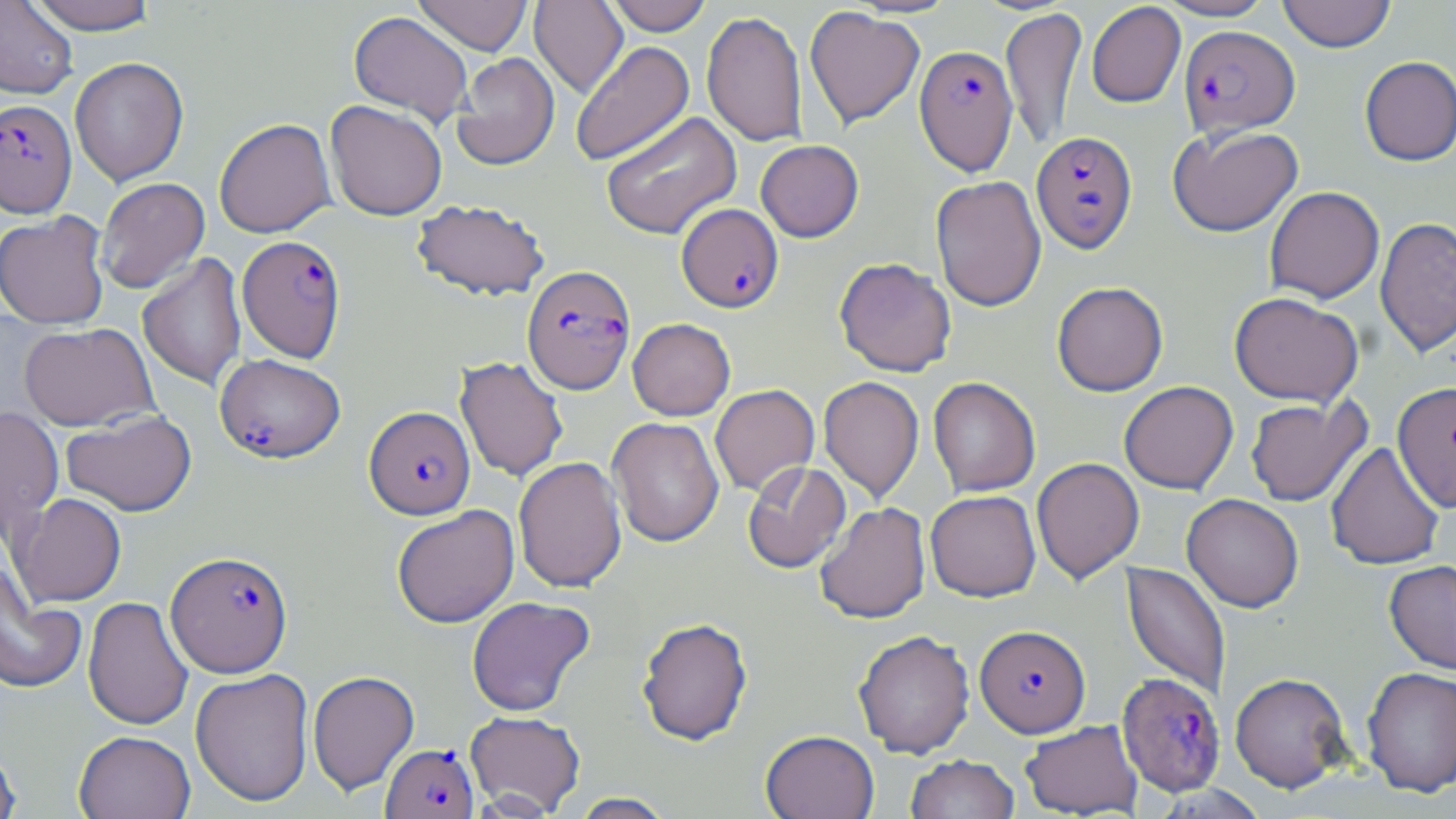

slide-level diagnosis = Plasmodium falciparum
stain = May-Grünwald-Giemsa
modality = optical microscopy
uninfected red blood cell locations = approximate bounding boxes as [x1, y1, x2, y2] in pixels: [25, 0, 160, 34], [413, 0, 533, 56], [529, 0, 628, 99], [604, 0, 712, 36], [1155, 0, 1277, 21], [1277, 0, 1396, 53], [0, 1, 77, 99], [1086, 2, 1186, 108], [804, 6, 925, 130], [1000, 7, 1086, 150], [701, 10, 808, 147], [348, 11, 473, 125], [570, 41, 694, 166], [452, 52, 559, 170], [1359, 56, 1456, 166], [70, 57, 188, 186], [325, 100, 447, 221], [601, 112, 742, 240], [214, 118, 336, 238], [1167, 124, 1303, 237], [755, 140, 864, 242], [930, 175, 1046, 312], [96, 177, 210, 293], [1264, 186, 1384, 304], [411, 198, 550, 301], [0, 211, 111, 329], [1375, 216, 1456, 358], [137, 253, 247, 390], [834, 257, 957, 377], [1052, 281, 1168, 396], [1229, 291, 1363, 407], [627, 318, 735, 420], [19, 322, 157, 431], [455, 356, 568, 482], [818, 376, 924, 503], [928, 376, 1041, 497], [1119, 381, 1238, 494], [1392, 381, 1456, 513], [710, 384, 819, 496], [1245, 396, 1370, 506], [0, 406, 63, 540], [61, 410, 196, 517], [607, 416, 724, 547], [1326, 441, 1445, 570], [513, 456, 627, 593], [1031, 457, 1144, 585], [743, 460, 851, 573], [925, 490, 1041, 602], [12, 493, 127, 607], [1181, 493, 1304, 612], [814, 502, 931, 624], [391, 504, 519, 628], [0, 560, 87, 695], [1384, 560, 1456, 674], [1121, 562, 1230, 700], [83, 596, 193, 731], [466, 596, 595, 717], [636, 617, 753, 746], [853, 630, 975, 758], [1361, 666, 1456, 797], [190, 668, 314, 806], [307, 670, 419, 795], [1230, 672, 1352, 793], [465, 710, 585, 815], [1020, 719, 1143, 818], [73, 730, 195, 819], [760, 730, 880, 818], [0, 745, 21, 819], [905, 755, 1020, 819], [570, 792, 676, 818]
preparation = thin blood smear
field of view = one of a larger specimen
Plasmodium falciparum-infected red blood cell locations = approximate bounding boxes as [x1, y1, x2, y2] in pixels: [1179, 26, 1300, 138], [914, 44, 1018, 176], [0, 99, 77, 217], [1031, 131, 1138, 253], [677, 203, 783, 313], [237, 235, 347, 362], [522, 265, 635, 395], [215, 353, 345, 463], [364, 406, 475, 519], [166, 551, 293, 677], [975, 624, 1090, 737], [1116, 672, 1226, 796], [381, 743, 478, 819]
magnification = 1000x
image size = 1456×819 pixels